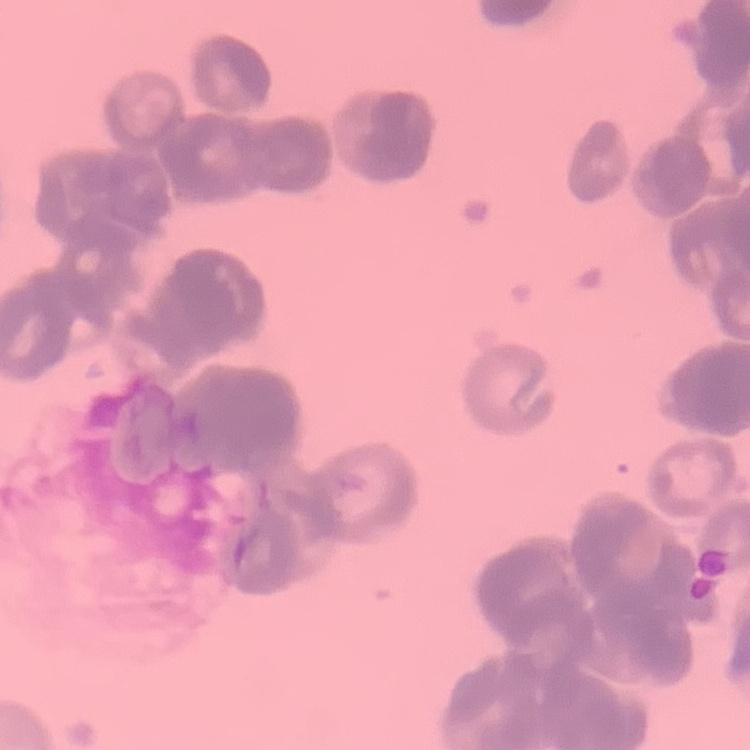

Summary:
  - Red blood cell morphology: rouleaux formation
  - Preparation: thin blood smear
  - Image type: square crop of a larger photomicrograph
  - Stain: Field's or Giemsa